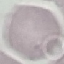
Summary:
  - Malaria status: uninfected
  - Preparation: thin blood film
  - Capture: smartphone through the microscope eyepiece
  - Stain: Giemsa
  - Image type: automatically extracted cell patch, resized to 64 × 64 pixels